Assess the morphology of the red blood cells.
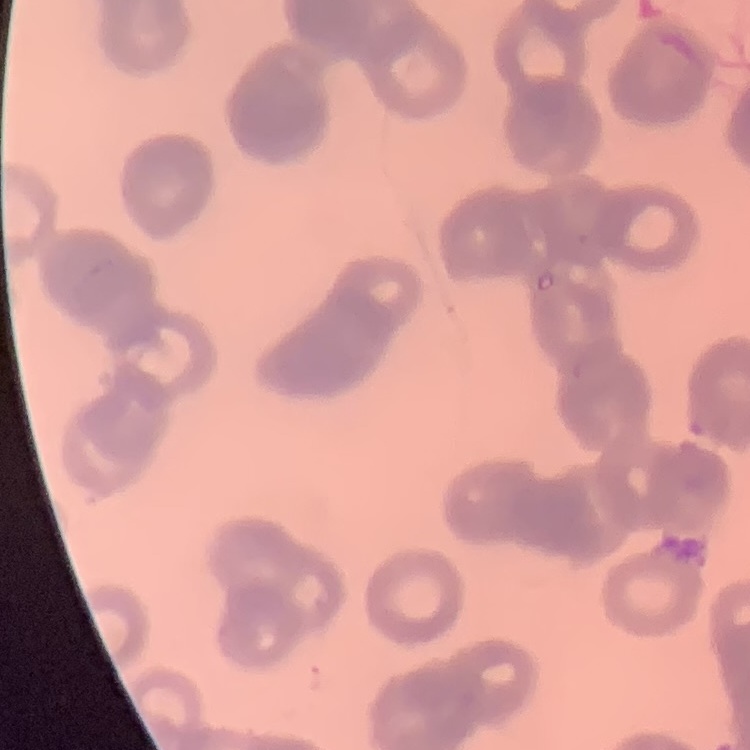
They show rouleaux formation.

Summary:
  - Image type: one tile cut from a larger photomicrograph
  - Stain: Field's or Giemsa
  - Preparation: thin peripheral smear